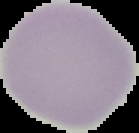 From a thin blood smear. Cell region segmented out of the field of view; the surrounding area is masked to black. Image is 139×133 pixels. Result: no Plasmodium parasites seen.